Identify the parasite.
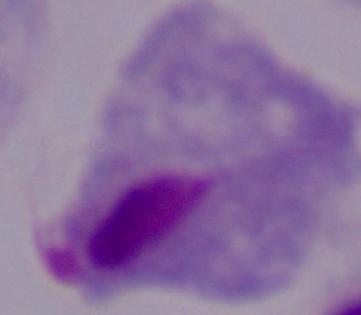
A trichomonad.

1000x magnification. Micrograph.